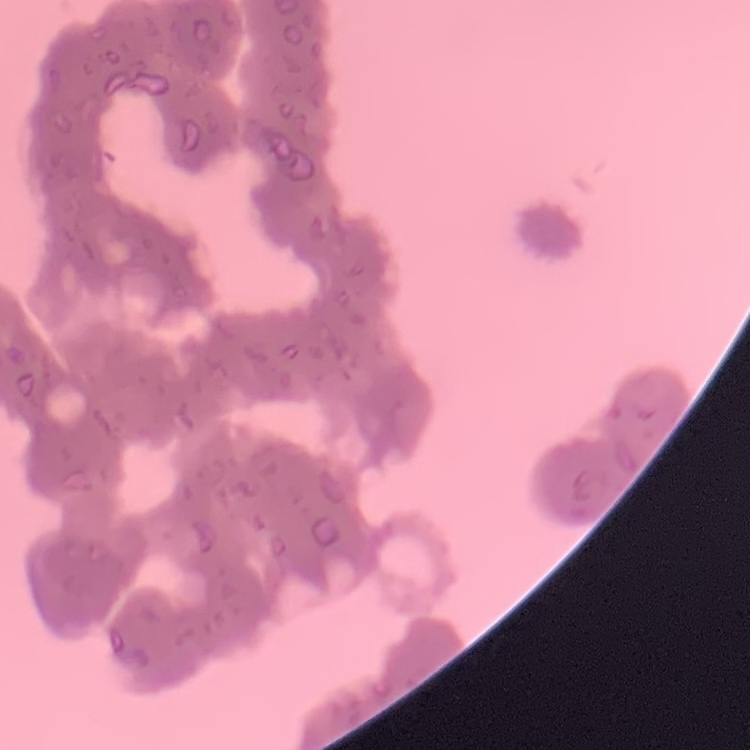 The red blood cells show rouleaux formation. One tile cut from a larger photomicrograph. Thin blood smear. Stained with either Field's or Giemsa.